Point out each Plasmodium parasite.
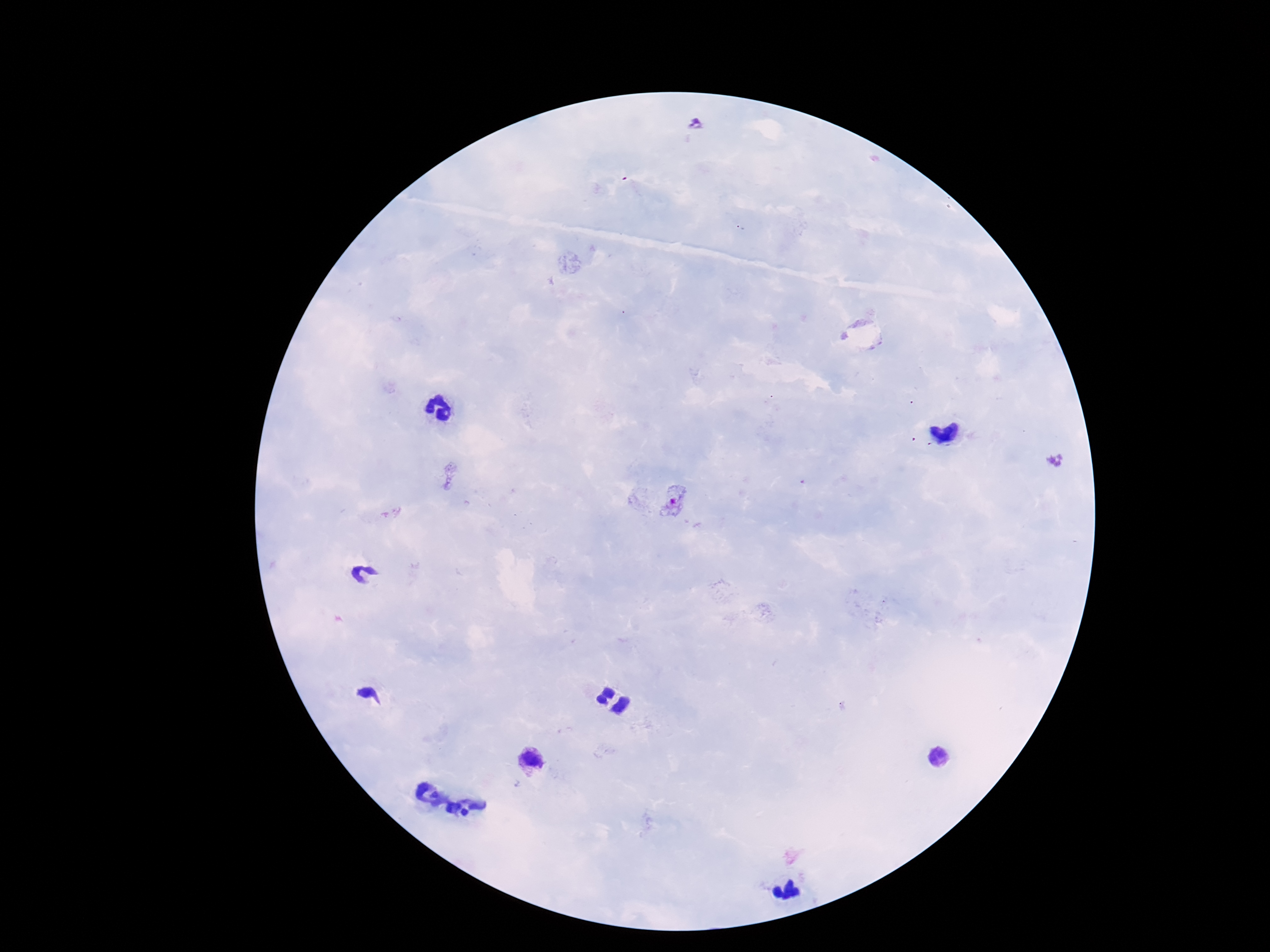
Approximate centers as [x, y] in pixels.
Plasmodium parasites: [695, 125], [676, 504], [531, 761].

Summary:
  - Magnification: 100x
  - Image size: 1270×952 pixels
  - Capture: smartphone camera through the microscope eyepiece
  - Stain: Giemsa
  - Preparation: thick peripheral-blood smear
  - Field of view: single
  - Patient malaria status: infected